Report the malaria status of this cell.
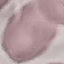

It is uninfected.

Thin blood smear. Giemsa-stained preparation. Automatically extracted cell patch, resized to 64 × 64 pixels. Photographed with a smartphone camera at the microscope eyepiece.